Classify this cell by malaria status.
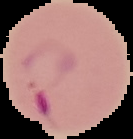

Parasitized.

Summary:
  - Preparation: thin blood film
  - Image type: cell region segmented out of the field of view; surrounding area masked to black
  - Image size: 133×139 pixels